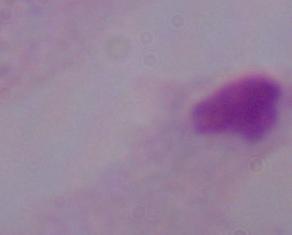
{
  "identification": "trichomonad",
  "magnification": "1000x",
  "modality": "photomicrograph"
}